Classify this cell by malaria status.
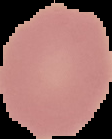

It is uninfected.

From a thin blood film. Image is 112×139 pixels. Cell region segmented out of the field of view; the surrounding area is masked to black.